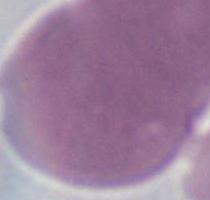

An erythrocyte is seen. Micrograph. Captured at 1000x magnification.